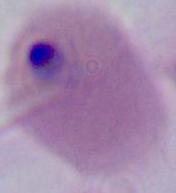

{
  "modality": "photomicrograph",
  "magnification": "400x or 1000x",
  "identification": "Plasmodium"
}